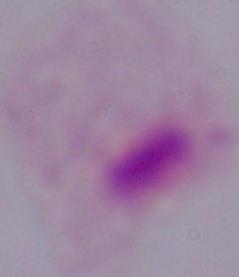

{
  "identification": "trichomonad",
  "modality": "micrograph",
  "magnification": "1000x"
}